Identify the blood parasite species.
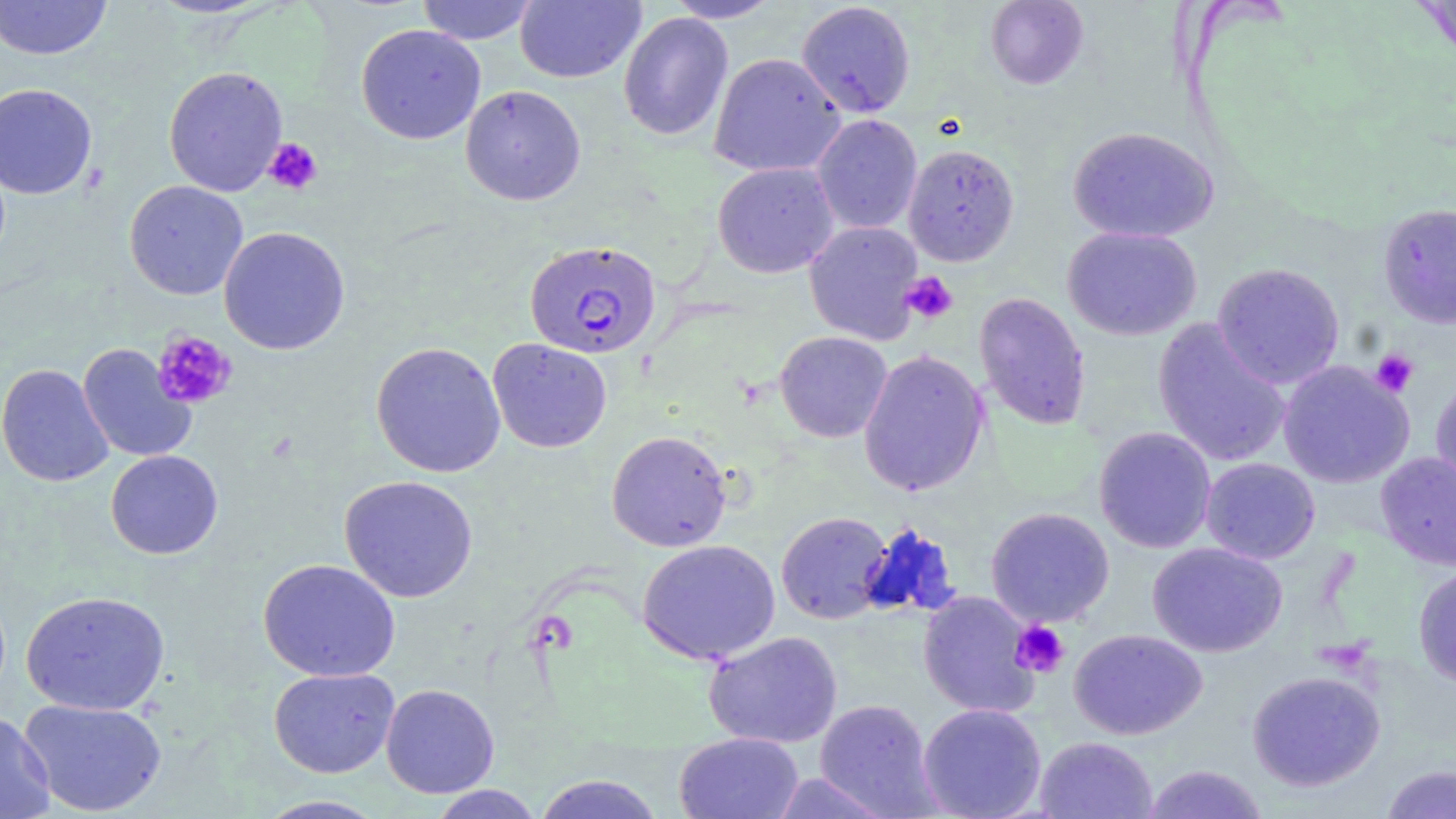

Plasmodium falciparum.

Summary:
  - Coordinate format: approximate bounding boxes as (x1, y1, x2, y2) in pixels
  - Plasmodium falciparum-infected red blood cell locations: (525, 240, 661, 360)
  - Platelet locations: (263, 138, 322, 195), (901, 272, 958, 324), (152, 330, 237, 410), (1370, 349, 1419, 397), (1010, 620, 1069, 677)
  - Uninfected red blood cell locations: (0, 0, 113, 60), (416, 0, 540, 45), (514, 0, 646, 84), (665, 0, 783, 23), (986, 0, 1088, 89), (1413, 0, 1456, 65), (796, 1, 915, 118), (617, 12, 734, 141), (355, 23, 486, 145), (709, 52, 846, 178), (163, 65, 288, 197), (0, 82, 97, 199), (460, 84, 586, 206), (811, 114, 923, 234), (1068, 126, 1219, 244), (903, 143, 1020, 266), (712, 162, 838, 278), (124, 180, 248, 300), (1378, 202, 1456, 329), (804, 221, 924, 344), (218, 226, 350, 355), (1062, 226, 1202, 341), (1212, 262, 1345, 389), (973, 292, 1091, 430), (1152, 318, 1292, 467), (774, 331, 892, 443), (487, 338, 613, 453), (371, 341, 506, 478), (77, 343, 196, 463), (858, 349, 989, 497), (1278, 360, 1414, 488), (0, 363, 114, 487), (1431, 377, 1456, 494), (1093, 427, 1216, 553), (606, 430, 732, 552), (105, 450, 223, 559), (1376, 452, 1456, 570), (1201, 458, 1320, 564), (339, 475, 478, 603), (986, 507, 1114, 626), (776, 511, 893, 624), (857, 522, 961, 621), (637, 539, 780, 665), (1147, 542, 1288, 657), (258, 558, 400, 682), (1412, 566, 1456, 688), (20, 590, 171, 715), (917, 591, 1041, 718), (1069, 629, 1207, 740), (703, 630, 843, 749), (268, 667, 400, 778), (1246, 669, 1386, 791), (381, 683, 499, 798), (18, 697, 168, 817), (814, 699, 940, 816), (917, 703, 1046, 819), (0, 713, 55, 819), (674, 732, 804, 819), (1034, 736, 1157, 818), (1142, 764, 1269, 819), (1381, 764, 1456, 819), (769, 772, 894, 819), (532, 774, 666, 819), (427, 784, 544, 818), (254, 795, 390, 818)
  - Preparation: thin blood film
  - Modality: light microscopy
  - Stain: May-Grünwald-Giemsa
  - Image size: 1456×819 pixels
  - Magnification: 1000x
  - Field of view: single